Locate every malaria parasite and identify its life-cycle stage.
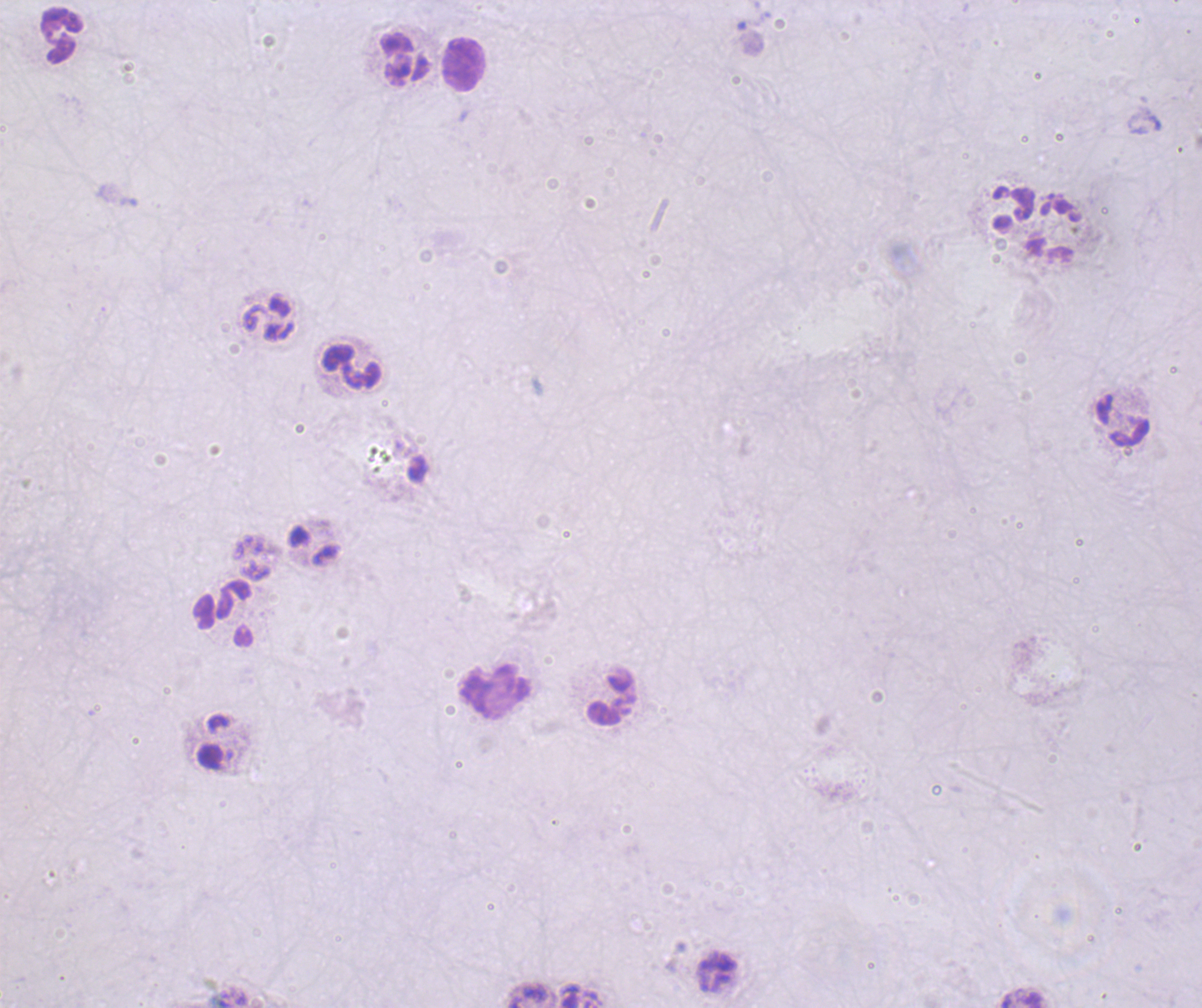
Negative for malaria parasites.

Approximate centers as [x, y] in pixels.
Summary:
  - Leukocyte locations: [61, 35], [405, 60], [463, 65], [350, 367], [1122, 421], [314, 544], [226, 615], [494, 691], [612, 696]
  - Context: previously used in an actual diagnosis
  - Image size: 1202×1008 pixels
  - Magnification: 100x
  - Coloration quality: bad
  - Field of view: one from this slide
  - Stain: Romanowsky
  - Preparation: thick blood film
  - Background quality: unsatisfactory